Give the extent of all Plasmodium vivax-infected red blood cells.
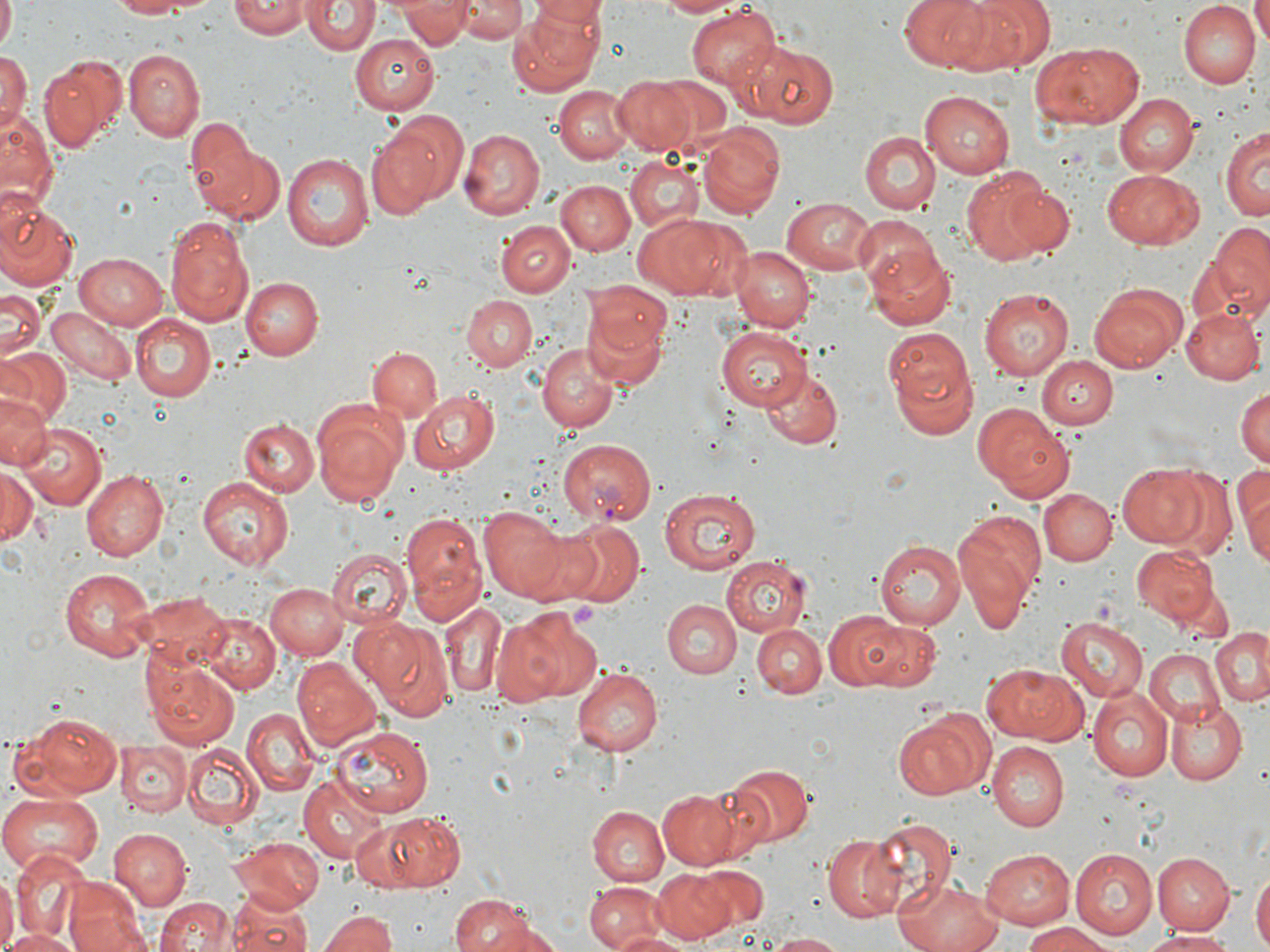
Approximate bounding boxes as [x1, y1, x2, y2] in pixels.
Plasmodium vivax-infected red blood cells: [556, 436, 659, 525].

Uninfected red blood cell locations: [0, 0, 16, 48], [106, 0, 223, 17], [231, 0, 310, 38], [398, 0, 473, 49], [528, 0, 604, 33], [651, 0, 739, 17], [898, 0, 997, 73], [948, 0, 1057, 72], [1253, 0, 1270, 45], [302, 1, 377, 56], [457, 1, 527, 42], [516, 1, 604, 91], [1178, 2, 1258, 87], [685, 6, 779, 90], [353, 33, 440, 114], [1031, 42, 1143, 128], [741, 43, 841, 129], [0, 47, 29, 133], [124, 51, 205, 140], [40, 53, 127, 151], [647, 76, 737, 155], [613, 77, 700, 155], [554, 85, 634, 163], [923, 88, 1016, 178], [1113, 93, 1196, 177], [1, 109, 53, 202], [184, 114, 264, 211], [365, 116, 460, 219], [1221, 123, 1269, 221], [695, 126, 782, 218], [460, 128, 543, 218], [860, 131, 939, 214], [201, 142, 286, 226], [281, 152, 374, 253], [626, 156, 704, 232], [962, 169, 1056, 266], [1101, 169, 1205, 250], [556, 179, 636, 256], [1000, 181, 1076, 255], [780, 195, 878, 275], [0, 202, 78, 291], [631, 212, 745, 299], [165, 214, 255, 328], [853, 215, 943, 301], [496, 221, 574, 297], [1193, 225, 1270, 326], [865, 244, 957, 331], [731, 246, 813, 332], [75, 253, 168, 329], [240, 277, 321, 359], [1089, 282, 1187, 371], [0, 286, 47, 360], [978, 288, 1074, 380], [462, 294, 537, 369], [583, 301, 671, 389], [1181, 306, 1264, 383], [49, 307, 134, 385], [132, 314, 214, 402], [718, 327, 810, 411], [883, 330, 978, 439], [537, 344, 619, 432], [368, 346, 442, 425], [0, 347, 70, 428], [1035, 356, 1116, 428], [759, 365, 843, 449], [1234, 383, 1270, 467], [409, 389, 501, 475], [0, 394, 50, 471], [311, 401, 408, 508], [976, 402, 1075, 502], [237, 417, 319, 496], [16, 423, 107, 509], [1234, 461, 1269, 565], [1118, 463, 1211, 547], [0, 467, 39, 545], [81, 469, 168, 560], [199, 476, 295, 571], [661, 486, 763, 575], [1040, 489, 1115, 566], [476, 504, 577, 603], [399, 509, 485, 617], [955, 509, 1046, 614], [549, 519, 643, 609], [518, 524, 607, 607], [875, 538, 967, 627], [1131, 545, 1217, 626], [328, 548, 411, 628], [721, 555, 809, 637], [59, 567, 156, 659], [266, 582, 348, 658], [134, 592, 232, 669], [436, 599, 508, 699], [663, 599, 742, 678], [504, 608, 595, 702], [823, 610, 907, 690], [199, 614, 278, 693], [1056, 617, 1147, 701], [358, 618, 452, 720], [865, 620, 939, 690], [754, 622, 826, 699], [1210, 629, 1270, 706], [1143, 650, 1224, 726], [294, 657, 383, 752], [148, 660, 241, 750], [982, 661, 1086, 745], [572, 668, 663, 756], [1089, 688, 1173, 780], [1166, 700, 1247, 783], [240, 709, 320, 794], [893, 710, 992, 800], [16, 712, 123, 798], [331, 723, 437, 816], [116, 741, 191, 816], [181, 742, 263, 830], [987, 742, 1066, 831], [727, 762, 813, 845], [298, 776, 388, 861], [657, 789, 743, 869], [0, 795, 101, 875], [586, 805, 668, 886], [362, 811, 468, 894], [864, 815, 956, 914], [109, 828, 192, 910], [819, 835, 903, 921], [231, 837, 323, 910], [979, 847, 1073, 929], [1070, 848, 1159, 941], [11, 853, 90, 940], [1153, 853, 1233, 932], [691, 864, 769, 932], [651, 869, 733, 945], [1253, 869, 1269, 952], [0, 870, 14, 952], [893, 877, 1004, 952], [62, 879, 148, 952], [586, 881, 669, 952], [226, 891, 314, 952], [449, 893, 548, 952], [156, 897, 236, 952], [317, 910, 400, 952], [1024, 922, 1114, 952], [2, 928, 84, 952], [1140, 928, 1240, 950], [610, 930, 688, 952], [766, 931, 846, 952]. Slide-level diagnosis: Plasmodium vivax. Image is 1270×952 pixels. 1000x magnification. Thin blood film. One field of a larger specimen. Light microscopy. May-Grünwald-Giemsa stain.